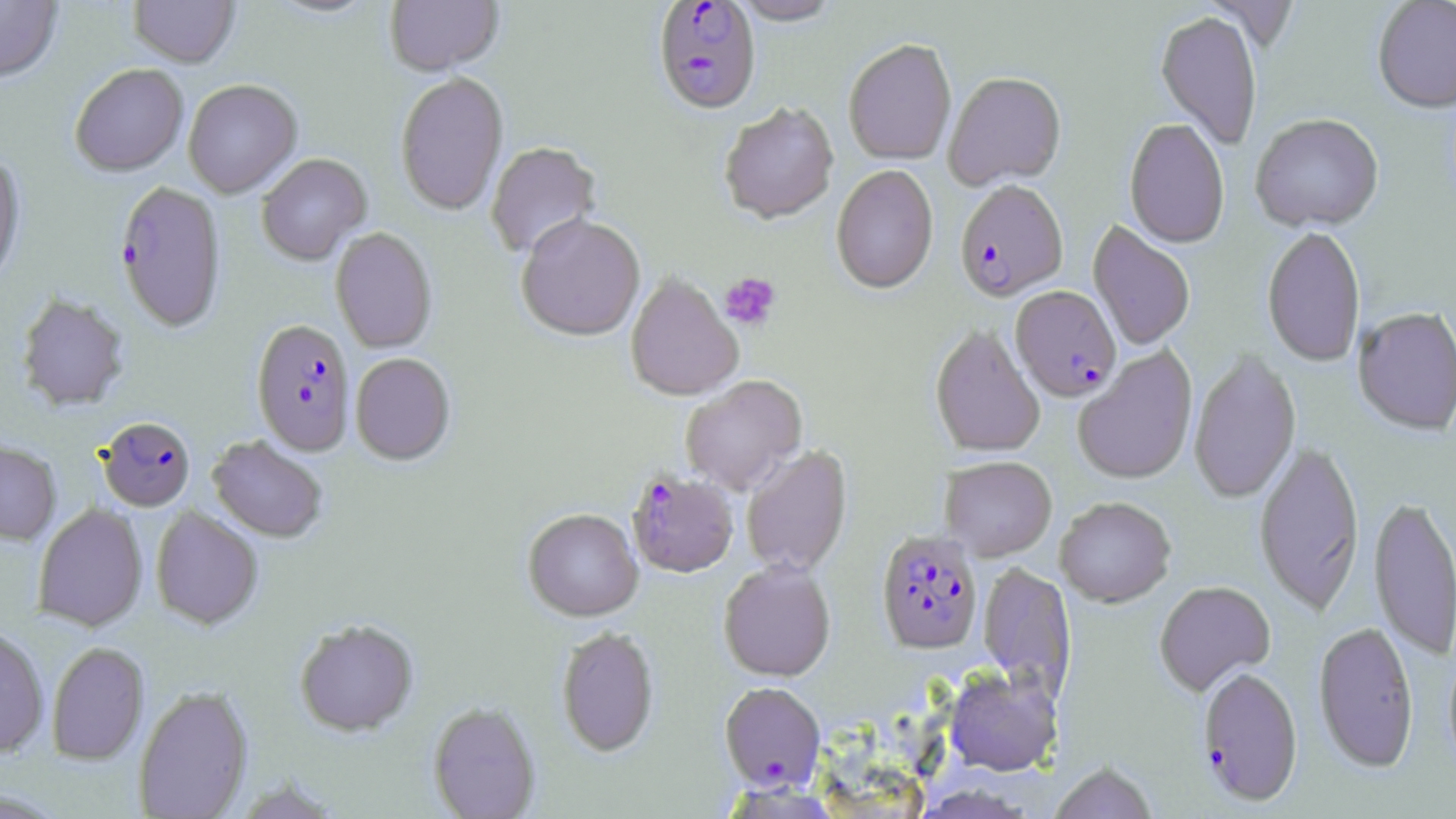
Summary:
  - Coordinate format: approximate bounding boxes as [x1, y1, x2, y2] in pixels
  - Uninfected red blood cell locations: [0, 0, 63, 86], [129, 0, 240, 69], [264, 0, 382, 20], [385, 0, 504, 77], [731, 0, 842, 27], [1372, 0, 1456, 115], [1155, 13, 1262, 150], [843, 41, 957, 166], [70, 64, 189, 177], [944, 73, 1067, 192], [395, 74, 509, 216], [184, 80, 302, 198], [719, 103, 839, 226], [1250, 116, 1384, 234], [1124, 119, 1229, 250], [485, 142, 602, 260], [257, 154, 371, 266], [0, 155, 26, 291], [830, 166, 939, 296], [517, 216, 646, 343], [1087, 221, 1195, 351], [1262, 227, 1366, 368], [331, 228, 437, 353], [626, 274, 743, 403], [16, 293, 130, 412], [1352, 308, 1456, 438], [930, 326, 1045, 458], [1073, 346, 1198, 485], [1188, 350, 1301, 505], [350, 353, 455, 466], [680, 376, 807, 496], [208, 436, 327, 543], [0, 441, 61, 544], [1254, 442, 1365, 616], [741, 446, 853, 577], [940, 457, 1057, 561], [1369, 495, 1456, 662], [1055, 497, 1176, 608], [32, 503, 148, 632], [150, 506, 263, 631], [523, 510, 643, 623], [719, 562, 836, 683], [978, 562, 1077, 701], [1154, 582, 1276, 698], [294, 620, 419, 737], [1313, 622, 1419, 775], [0, 626, 50, 757], [556, 628, 659, 758], [46, 642, 149, 766], [944, 668, 1062, 777], [134, 685, 253, 819], [427, 703, 541, 818], [1049, 763, 1157, 819]
  - Plasmodium falciparum-infected red blood cell locations: [652, 2, 762, 118], [114, 181, 227, 333], [954, 182, 1068, 303], [1010, 287, 1121, 403], [251, 320, 355, 457], [98, 416, 196, 512], [626, 470, 740, 579], [876, 531, 983, 657], [1196, 668, 1303, 807], [719, 683, 826, 791]
  - Platelet locations: [720, 272, 781, 330]
  - Slide-level diagnosis: Plasmodium falciparum
  - Preparation: thin blood film
  - Stain: May-Grünwald-Giemsa
  - Image size: 1456×819 pixels
  - Modality: optical microscopy
  - Field of view: single
  - Magnification: 1000x